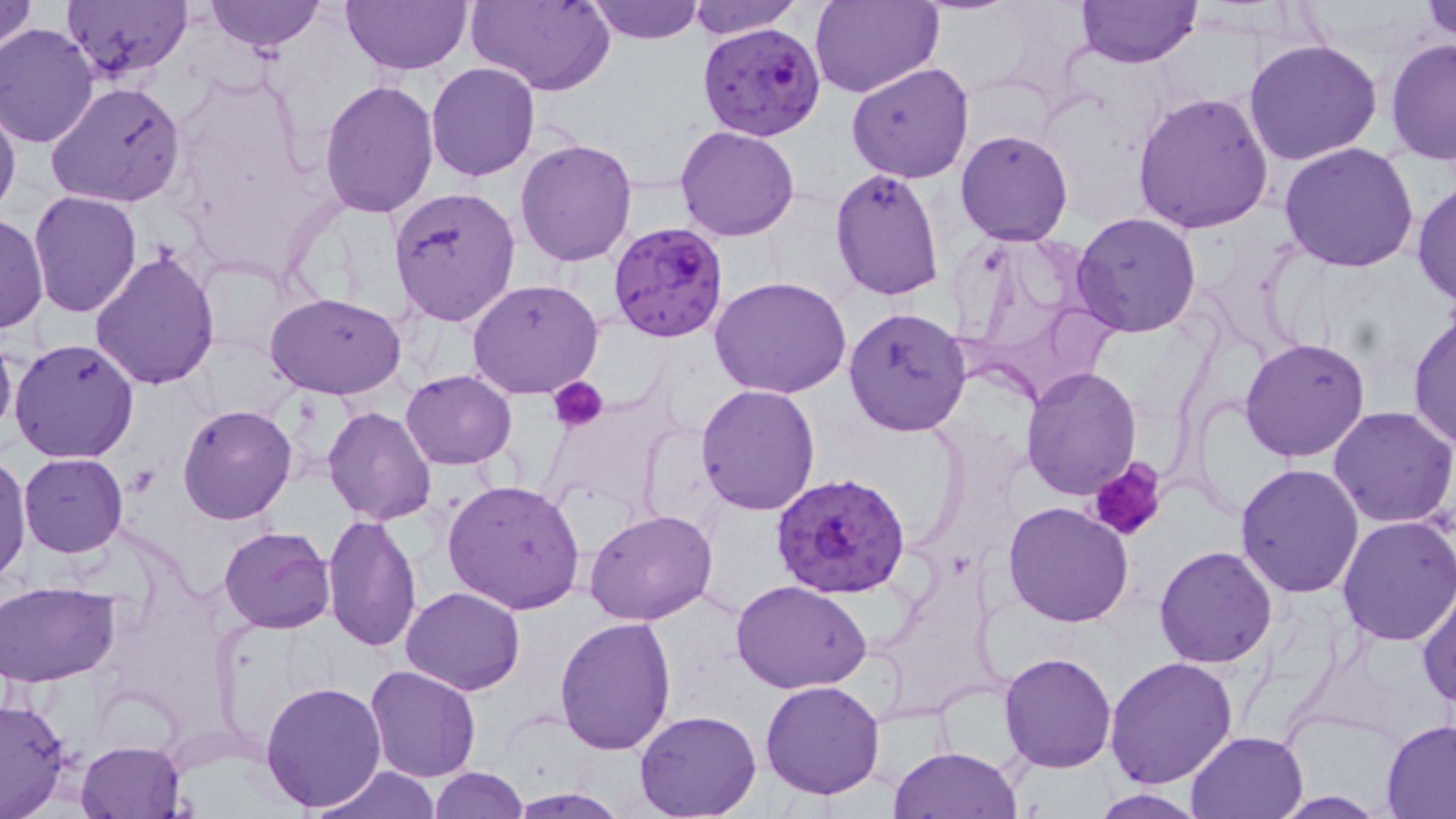

Approximate bounding boxes as (x1, y1, x2, y2) in pixels. Platelet locations: (550, 378, 609, 432), (1088, 456, 1171, 545). Uninfected red blood cell locations: (204, 0, 324, 53), (342, 0, 473, 74), (465, 0, 614, 95), (587, 0, 705, 43), (688, 0, 800, 37), (810, 0, 942, 99), (1074, 0, 1202, 68), (1422, 0, 1456, 43), (0, 1, 37, 52), (62, 1, 192, 85), (0, 23, 100, 148), (1385, 37, 1456, 165), (1243, 39, 1384, 166), (846, 61, 975, 184), (426, 63, 541, 183), (318, 78, 440, 219), (48, 81, 186, 207), (1132, 90, 1278, 234), (0, 99, 21, 222), (674, 123, 800, 242), (955, 128, 1073, 245), (515, 137, 638, 267), (1278, 142, 1420, 272), (829, 168, 945, 302), (1411, 179, 1456, 306), (390, 186, 522, 327), (29, 191, 142, 318), (1072, 212, 1202, 338), (1, 213, 48, 336), (946, 227, 1111, 395), (90, 251, 221, 393), (709, 276, 852, 399), (466, 280, 605, 399), (268, 292, 406, 399), (842, 304, 970, 435), (1407, 310, 1456, 450), (0, 332, 17, 444), (1239, 335, 1372, 463), (8, 337, 140, 464), (1020, 365, 1141, 501), (401, 370, 517, 469), (696, 385, 821, 515), (177, 404, 298, 526), (323, 406, 438, 526), (1328, 407, 1456, 529), (1, 450, 33, 584), (18, 452, 128, 557), (1235, 462, 1367, 597), (442, 478, 588, 615), (1001, 500, 1134, 628), (584, 510, 717, 626), (322, 513, 423, 653), (1335, 515, 1456, 648), (219, 527, 336, 634), (1154, 544, 1278, 667), (731, 579, 874, 695), (1, 581, 121, 685), (402, 586, 526, 695), (1417, 586, 1456, 710), (553, 618, 678, 756), (999, 651, 1118, 773), (1105, 657, 1239, 791), (365, 665, 482, 783), (259, 680, 388, 813), (759, 680, 885, 800), (0, 696, 74, 819), (635, 708, 762, 818), (1380, 718, 1456, 816), (1185, 729, 1310, 818), (76, 739, 186, 818), (889, 745, 1021, 819), (310, 765, 441, 819), (428, 766, 528, 817), (507, 787, 629, 817), (1089, 788, 1208, 818), (1269, 790, 1392, 817). Plasmodium falciparum-infected red blood cell locations: (698, 20, 827, 141), (606, 219, 729, 341), (772, 470, 912, 601). Slide-level diagnosis: Plasmodium falciparum. May-Grünwald-Giemsa-stained preparation. 1000x magnification. Light microscopy. Thin blood film. Image is 1456×819 pixels. One field of a larger specimen.